Name the parasite shown.
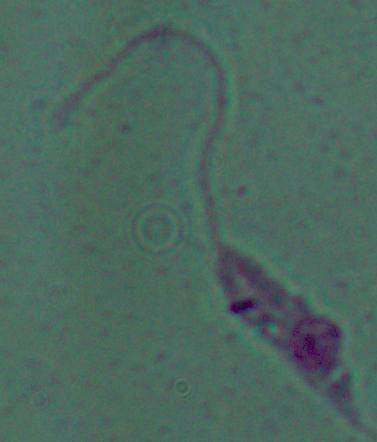

Leishmania.

Summary:
  - Magnification: 1000x
  - Modality: photomicrograph